Give the position of every malaria parasite and every leukocyte.
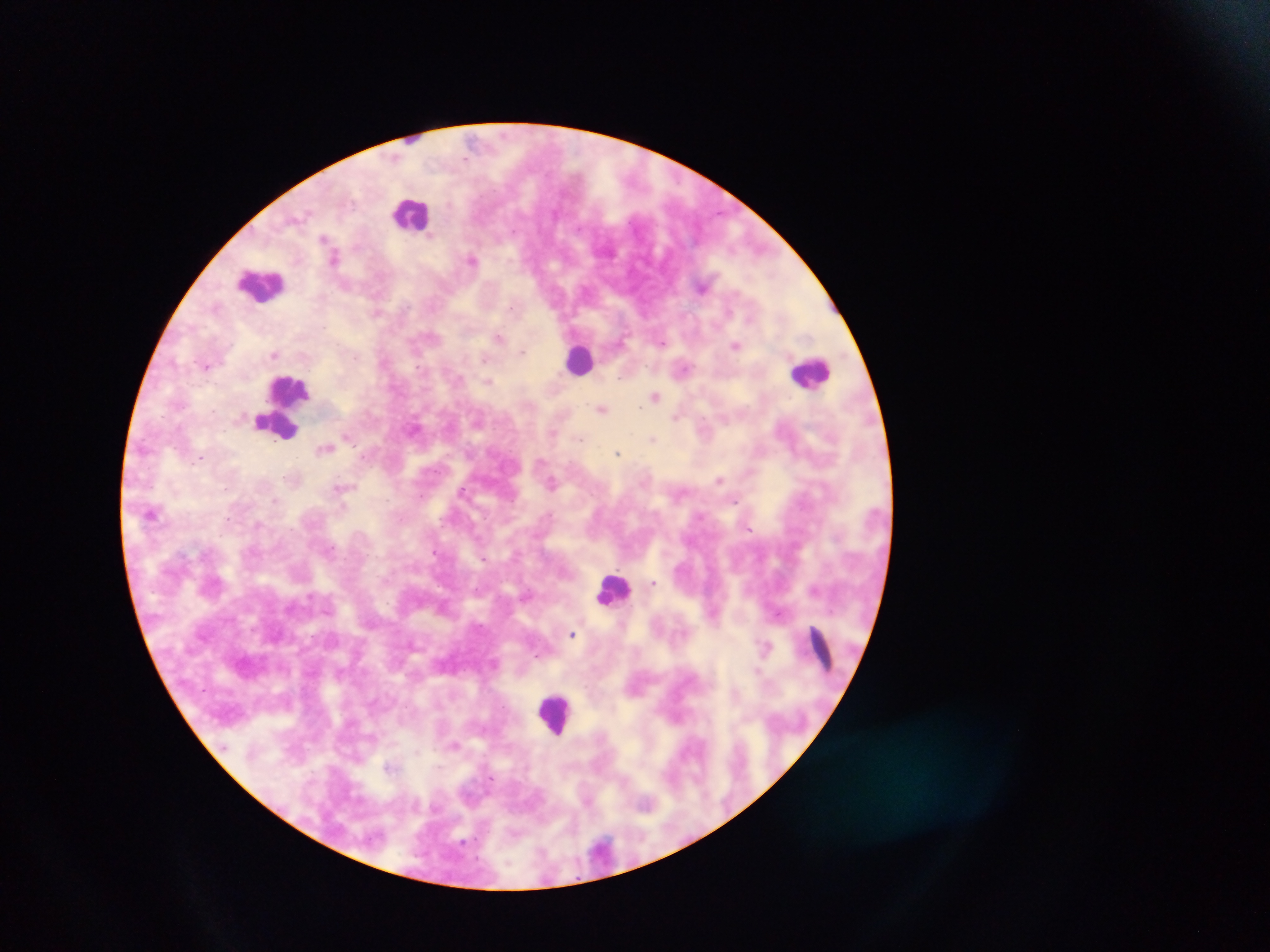
Approximate centers as {x, y} in pixels.
Malaria parasites: {324, 238}, {334, 258}, {473, 259}, {701, 287}, {215, 306}, {509, 308}, {376, 313}, {498, 337}, {662, 343}, {735, 345}, {523, 351}, {275, 354}, {485, 359}, {206, 365}, {683, 370}, {488, 382}, {655, 397}, {639, 407}, {601, 410}, {214, 412}, {676, 417}, {553, 434}, {348, 437}, {581, 439}, {652, 440}, {324, 448}, {618, 453}, {200, 458}, {720, 480}, {553, 483}, {342, 487}, {226, 488}, {463, 491}, {276, 500}, {735, 500}, {151, 512}, {548, 515}, {257, 524}, {749, 529}, {330, 548}, {434, 553}, {483, 558}, {653, 583}, {813, 591}, {572, 634}, {767, 647}, {822, 651}, {757, 671}, {454, 745}, {389, 767}, {601, 848}.
Leukocytes: {412, 212}, {261, 284}, {580, 359}, {811, 372}, {289, 391}, {278, 424}, {612, 588}, {556, 713}.

Collected in Ghana. Thick blood film. One field of view. Image is 1270×952 pixels. Mobile-phone photograph taken through the microscope.